Name the parasite shown.
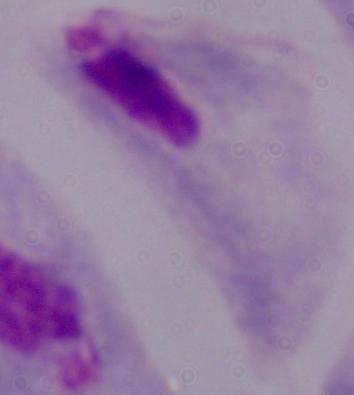

A trichomonad.

magnification = 1000x
modality = micrograph